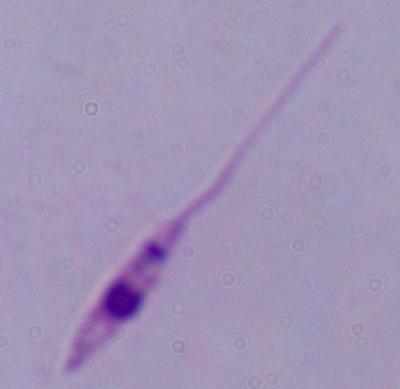
{
  "magnification": "1000x",
  "modality": "micrograph",
  "identification": "Leishmania"
}